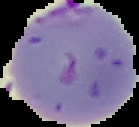

image type = segmented cell region on a black background
result = Plasmodium parasites detected
preparation = thin blood film
image size = 139×127 pixels